Assess the morphology of the red blood cells.
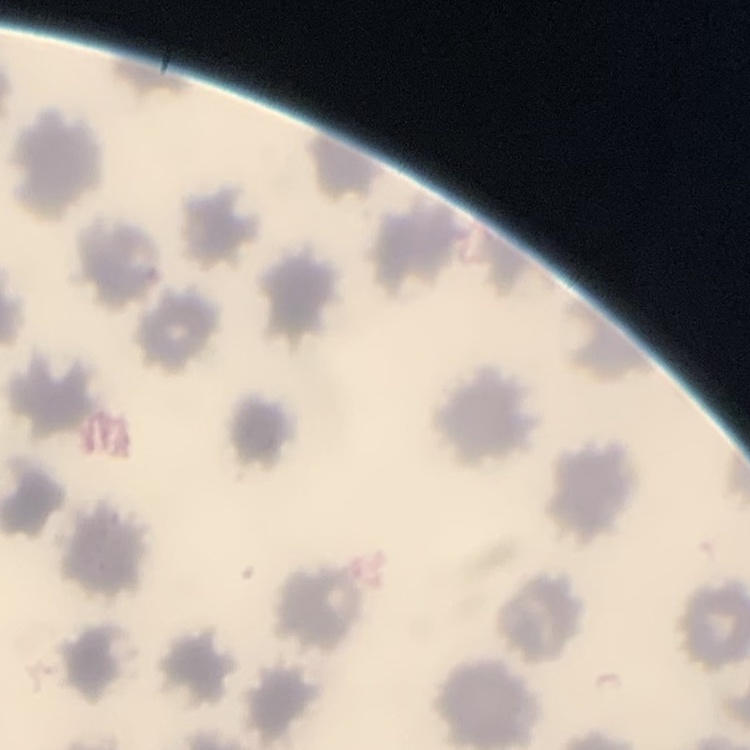
No rouleaux formation.

stain: Field's or Giemsa
preparation: thin peripheral smear
image_type: square crop of a larger photomicrograph